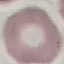

{
  "result": "negative for malaria parasites",
  "capture": "smartphone camera at the microscope eyepiece",
  "stain": "Giemsa",
  "image_type": "cell patch, automatically extracted from a larger field of view and resized to 64 × 64 pixels",
  "preparation": "thin blood film"
}